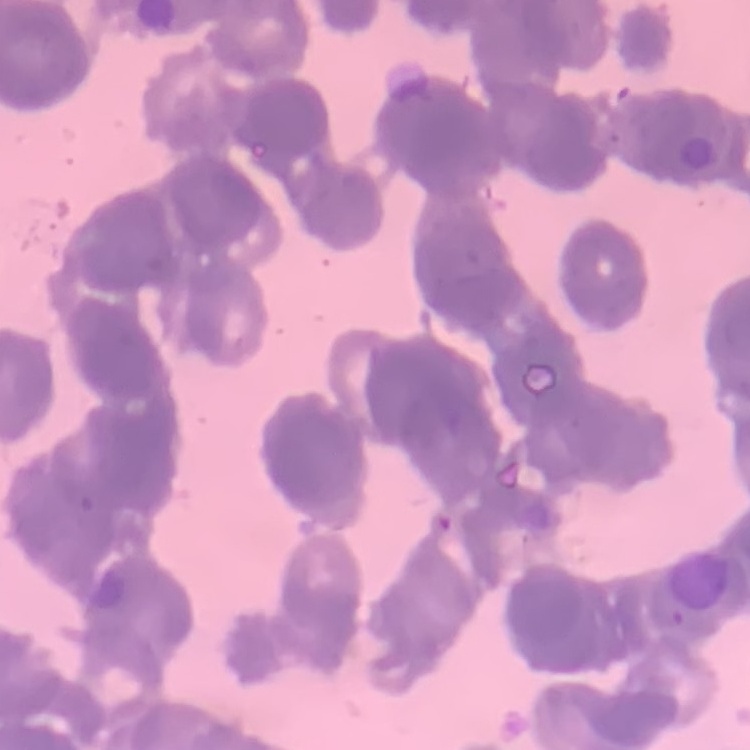

The erythrocytes exhibit rouleaux formation. Field's or Giemsa stain. Thin blood film. Square crop of a larger photomicrograph.